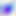
Summary:
  - Identification: Toxoplasma gondii
  - Magnification: 400x
  - Modality: micrograph